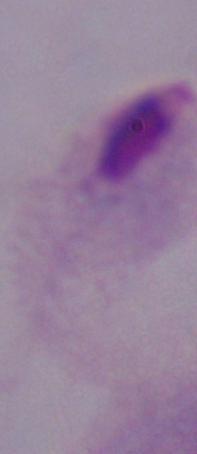
Micrograph. A trichomonad is seen. Captured at 1000x magnification.